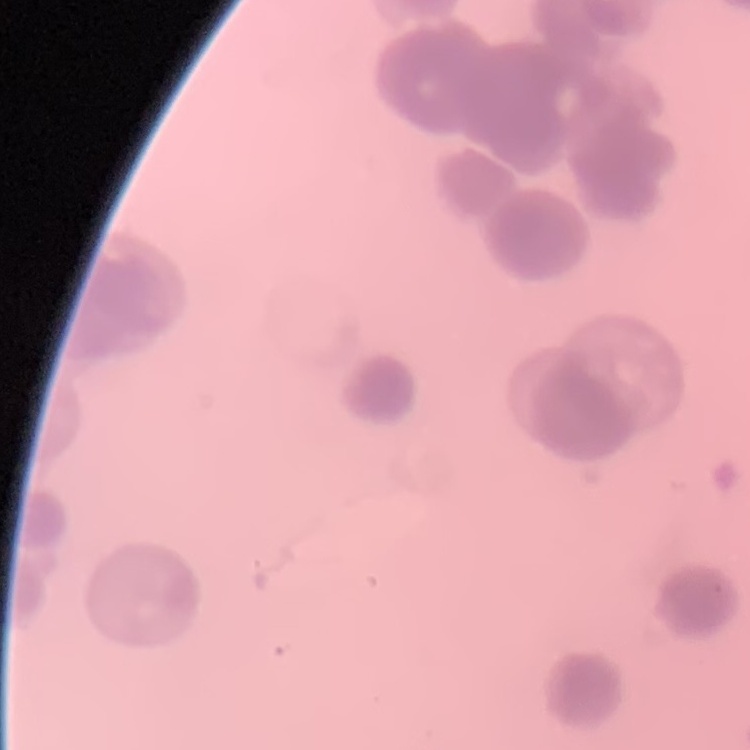
Summary:
  - Erythrocyte morphology: rouleaux formation
  - Stain: Field's or Giemsa
  - Image type: square crop of a larger photomicrograph
  - Preparation: thin peripheral smear